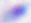

Photomicrograph. Captured at 400x magnification. Toxoplasma gondii is seen.